Assess the morphology of the erythrocytes.
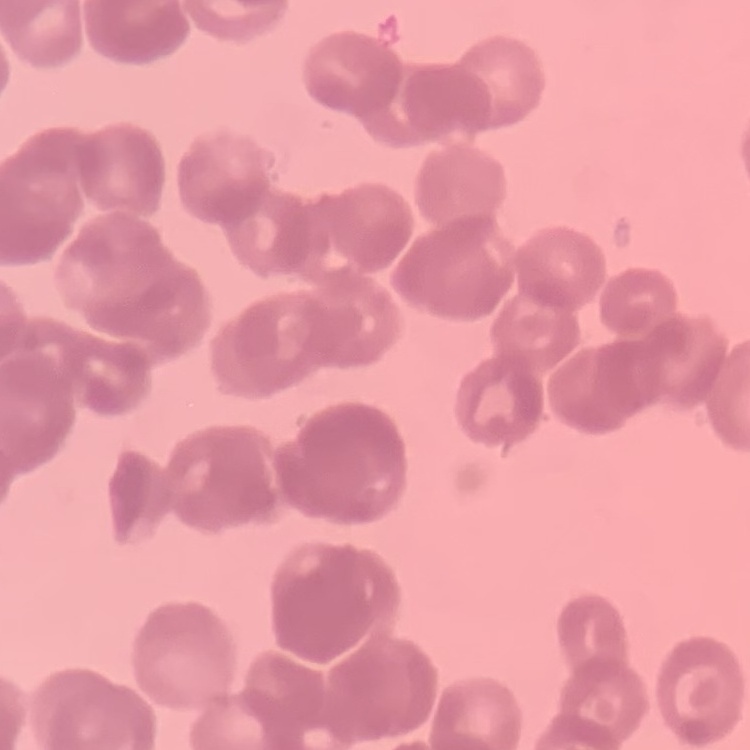

They show rouleaux formation.

Thin blood film. Stained with either Field's or Giemsa. One tile cut from a larger photomicrograph.